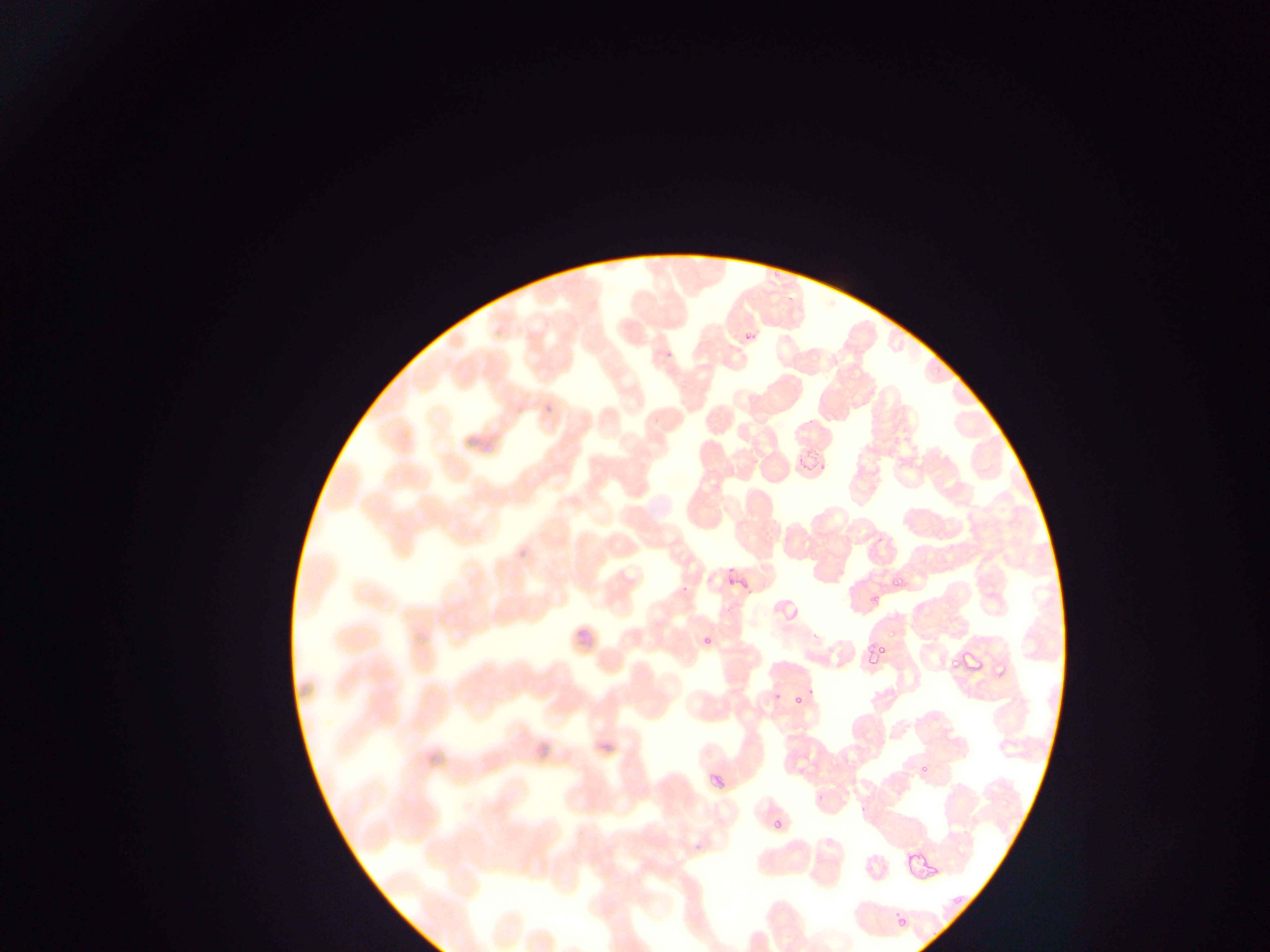 Approximate bounding boxes as left top right bottom in pixels. Malaria parasite locations: 742 316 761 344; 726 550 752 586; 892 576 905 591; 679 584 692 597; 865 591 882 614; 559 621 594 656; 700 630 717 648; 863 635 891 666; 954 642 995 685; 778 689 808 717; 724 745 762 776; 707 761 722 789; 773 810 785 844; 911 864 929 887; 896 912 908 926. Single field of view. Mobile-phone photograph taken through the microscope. Thin blood film. Sample from Ghana. Image is 1270×952 pixels.